Locate every leukocyte (white blood cell).
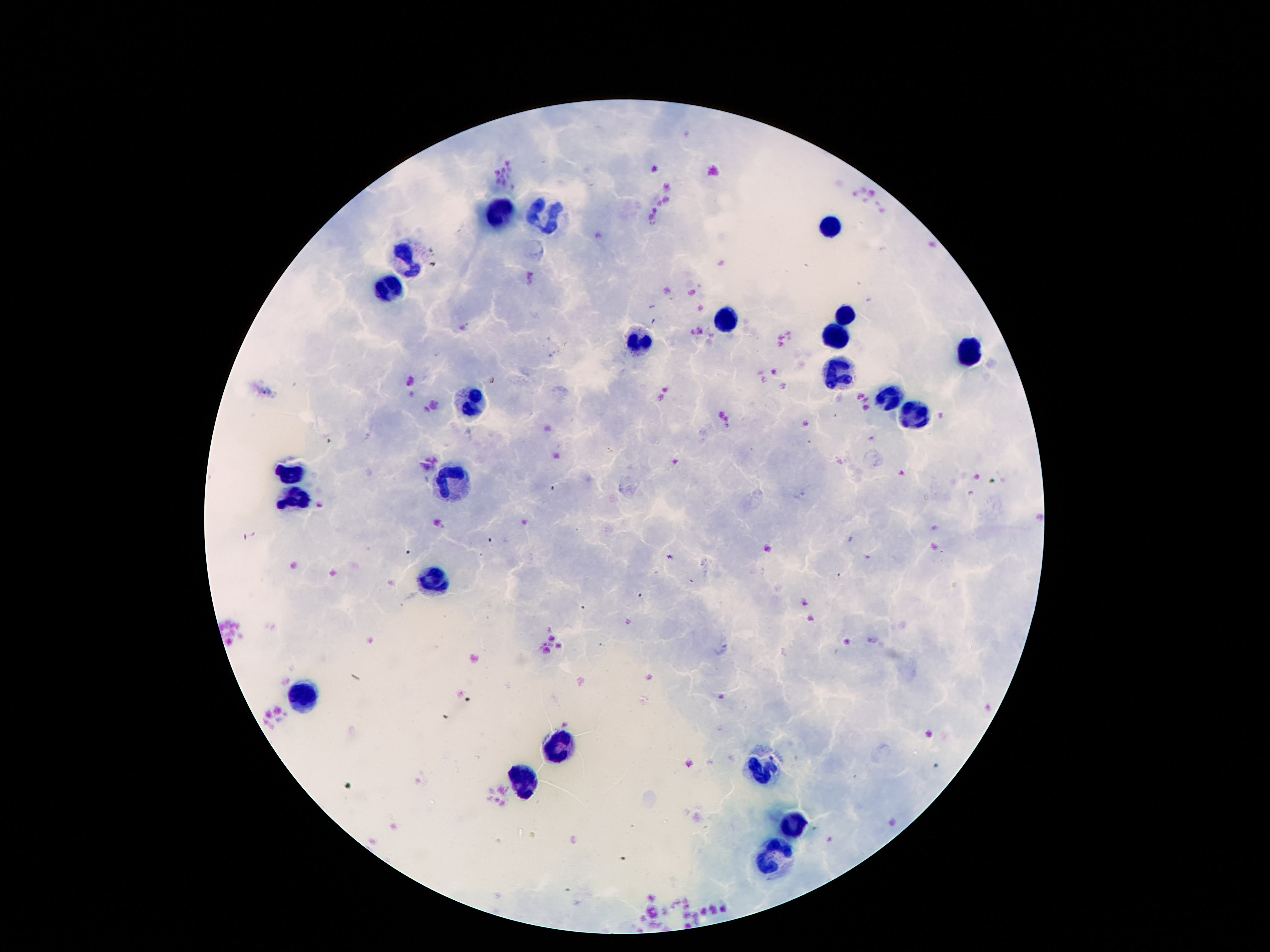

Approximate object centers, in pixels from the top-left corner.
Leukocytes: (x=500, y=215), (x=548, y=216), (x=838, y=224), (x=408, y=259), (x=392, y=287), (x=844, y=312), (x=730, y=321), (x=834, y=337), (x=640, y=344), (x=970, y=351), (x=838, y=372), (x=886, y=399), (x=472, y=404), (x=914, y=417), (x=294, y=470), (x=454, y=478), (x=298, y=498), (x=432, y=578), (x=296, y=700), (x=552, y=746), (x=766, y=772), (x=520, y=782), (x=794, y=826), (x=774, y=858).

Image is 1270×952 pixels. 100x magnification. Smartphone photograph taken through the microscope eyepiece. Thick peripheral-blood smear. One field from this slide. Giemsa-stained preparation. Patient malaria status: negative.